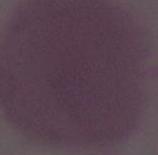

Photomicrograph. An erythrocyte is seen. Captured at 1000x magnification.